Evaluate for malaria.
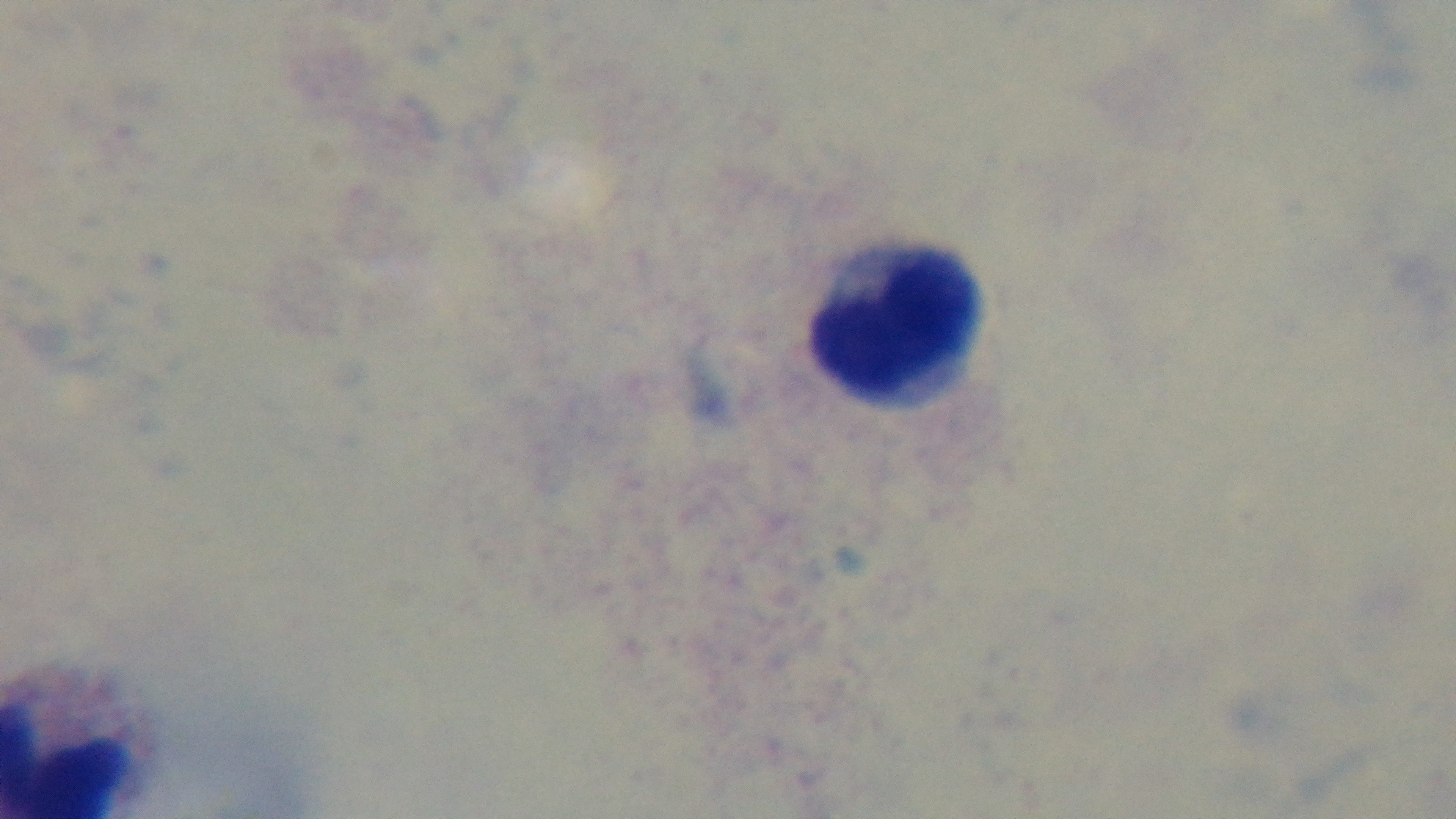
It is uninfected.

Oil-immersion objective, 100x. Captured with a mounted 4K digital camera. Preparation: thick smear. One field from the slide. Giemsa-stained. Photomicrograph.